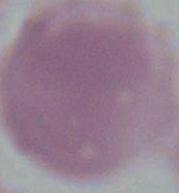
identification = red blood cell
magnification = 1000x
modality = micrograph